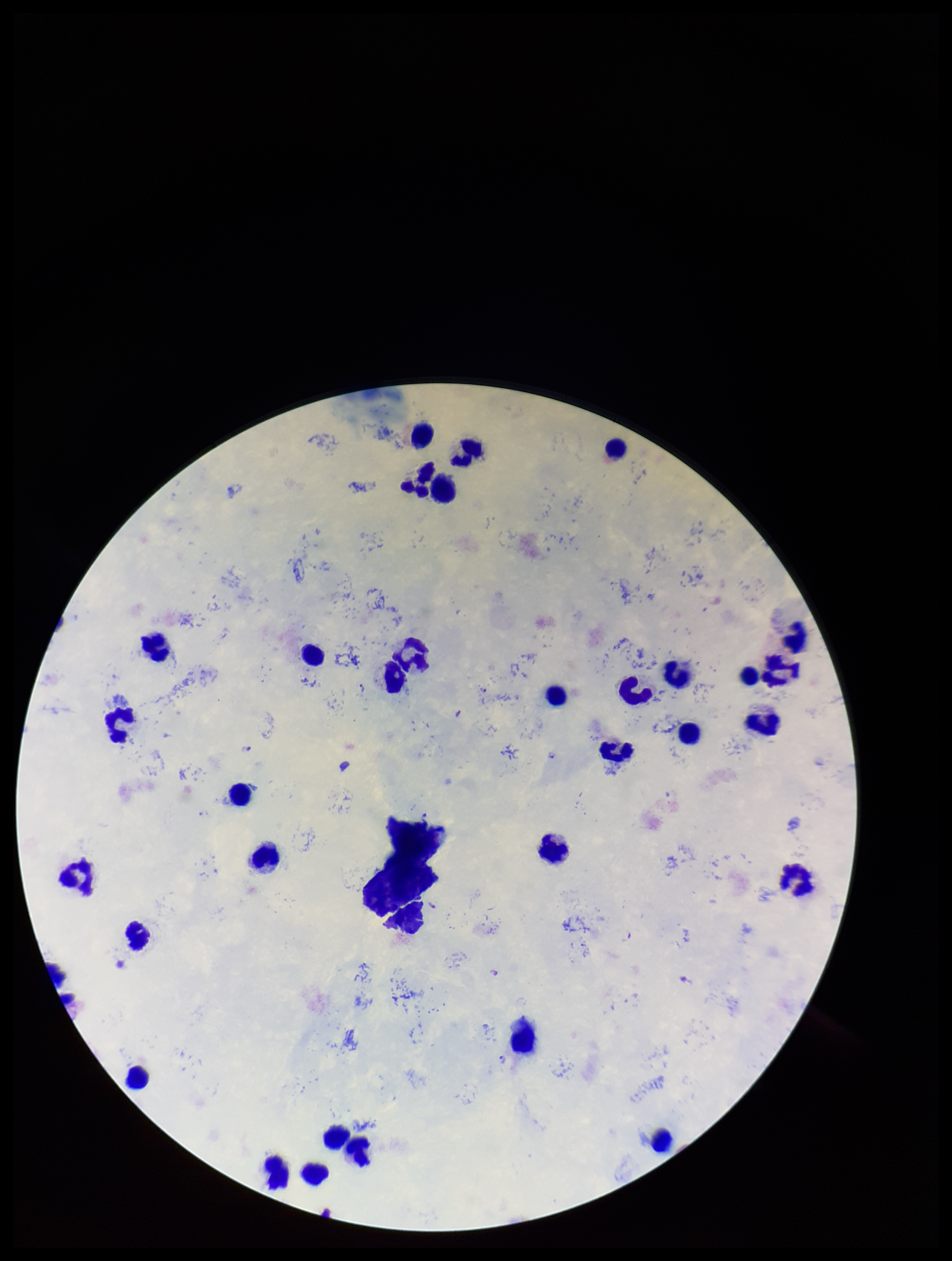
Preparation: thick. Plasmodium parasites: detected. Species reported for this patient: Plasmodium falciparum. Photographed through the microscope eyepiece with a smartphone camera. Patient malaria status: infected. Single field of view. Image is 952×1261 pixels. Stained with Giemsa. Parasite count: 4. Leukocyte count: 32.